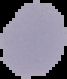

Image is 67×79 pixels. The area outside the segmented cell region is set to black. From a thin blood film. Result: no Plasmodium parasites detected.